Give the position of every Plasmodium parasite.
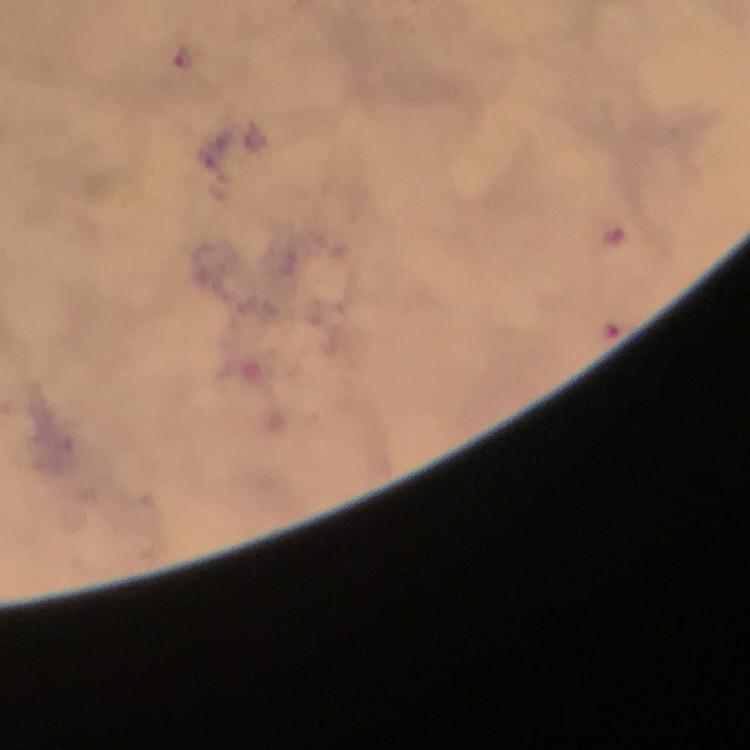

Approximate object centers, in pixels from the top-left corner.
Plasmodium parasites: (x=183, y=58).

Cropped region of a single field of view. At 100x magnification. Immersion oil was used. Giemsa-stained preparation. From a diagnostic examination for malaria. Photographed through the microscope with a smartphone camera. Thick blood film. Image is 750×750 pixels.